Name the blood parasite species.
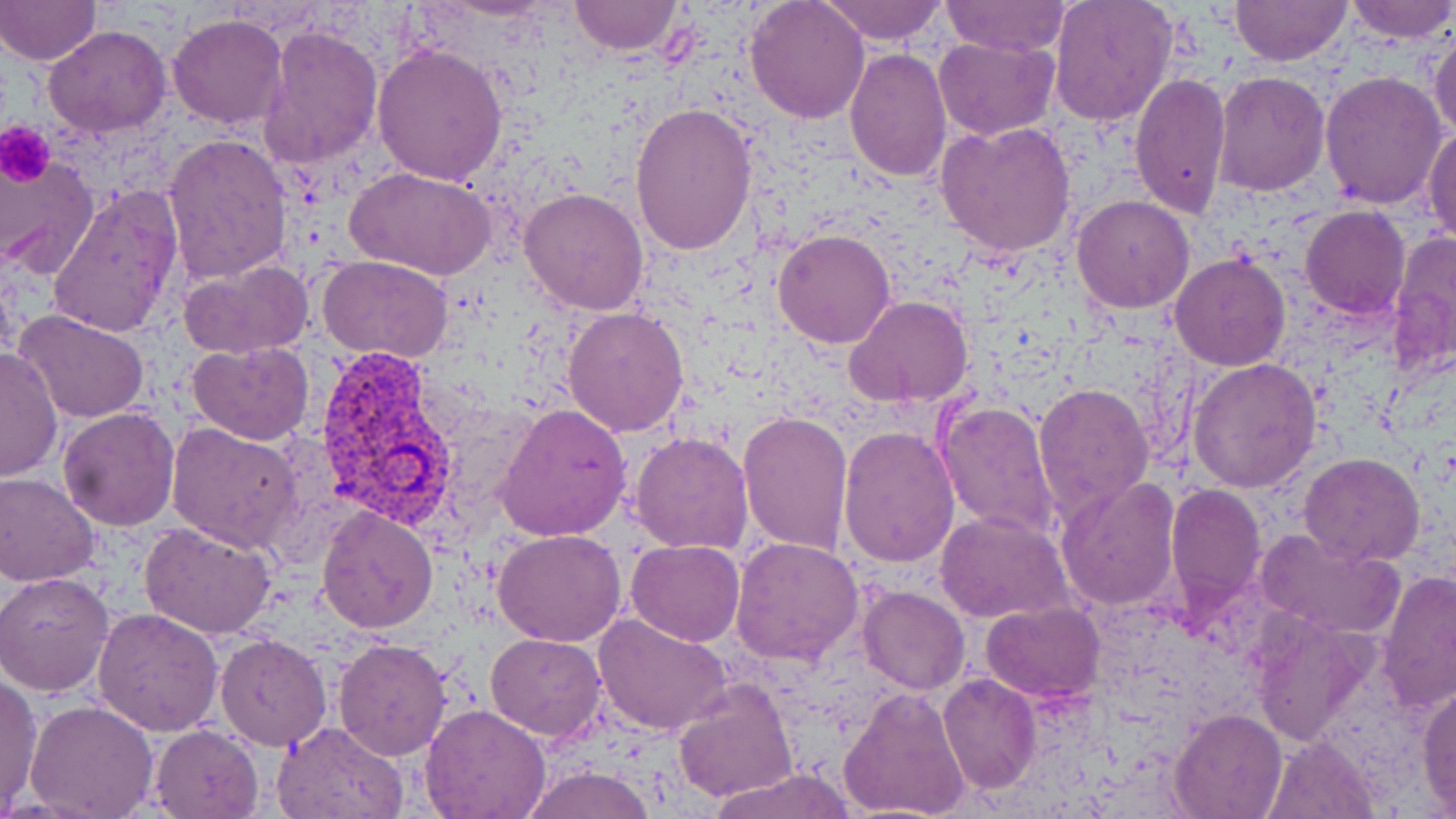
Plasmodium vivax.

field_of_view: single
platelet_locations: 'approximate bounding boxes as [x1, y1, x2, y2] in pixels: [1, 122, 54, 183]'
preparation: thin blood film
image_size: 1456×819 pixels
modality: optical microscopy
stain: May-Grünwald-Giemsa
uninfected_red_blood_cell_locations: 'approximate bounding boxes as [x1, y1, x2, y2] in pixels: [819, 0, 949, 46], [940, 0, 1072, 57], [1048, 0, 1179, 127], [1230, 0, 1349, 66], [1343, 0, 1456, 45], [567, 1, 683, 56], [746, 1, 870, 122], [0, 2, 101, 65], [167, 13, 289, 130], [258, 23, 383, 170], [44, 25, 173, 138], [1429, 27, 1456, 145], [934, 35, 1058, 139], [371, 41, 508, 184], [844, 47, 951, 182], [1211, 70, 1329, 195], [1127, 71, 1232, 219], [1319, 71, 1449, 210], [630, 102, 759, 257], [934, 120, 1078, 259], [1425, 125, 1456, 244], [163, 134, 293, 283], [0, 156, 101, 279], [346, 166, 497, 280], [45, 186, 184, 339], [520, 187, 649, 317], [1071, 194, 1196, 313], [1299, 205, 1410, 319], [772, 229, 894, 349], [1386, 232, 1455, 379], [1169, 253, 1291, 371], [318, 255, 455, 363], [179, 260, 314, 359], [845, 295, 973, 407], [563, 305, 691, 436], [15, 312, 149, 424], [187, 340, 314, 445], [1, 346, 62, 485], [1188, 359, 1322, 492], [1033, 381, 1155, 527], [935, 399, 1062, 543], [497, 402, 632, 542], [57, 408, 180, 531], [737, 411, 852, 554], [165, 424, 303, 556], [838, 426, 960, 567], [629, 432, 754, 554], [1299, 454, 1423, 566], [1, 471, 101, 585], [1056, 478, 1181, 612], [1164, 484, 1265, 611], [317, 506, 439, 632], [937, 510, 1073, 625], [140, 521, 278, 638], [492, 527, 626, 646], [1256, 527, 1404, 638], [729, 537, 864, 667], [626, 540, 744, 646], [1377, 569, 1456, 713], [1, 570, 116, 695], [858, 584, 969, 695], [980, 601, 1103, 702], [92, 606, 223, 737], [592, 612, 736, 736], [485, 633, 609, 740], [216, 634, 333, 752], [333, 636, 453, 759], [0, 671, 44, 807], [938, 673, 1041, 793], [672, 677, 799, 804], [1416, 682, 1456, 810], [840, 686, 972, 819], [25, 699, 158, 819], [421, 703, 551, 819], [1171, 707, 1286, 819], [271, 720, 409, 819], [150, 724, 262, 818], [1264, 733, 1383, 819], [520, 765, 656, 819], [706, 767, 858, 819]'
plasmodium_vivax_infected_red_blood_cell_locations: 'approximate bounding boxes as [x1, y1, x2, y2] in pixels: [314, 350, 457, 525]'
magnification: 1000x